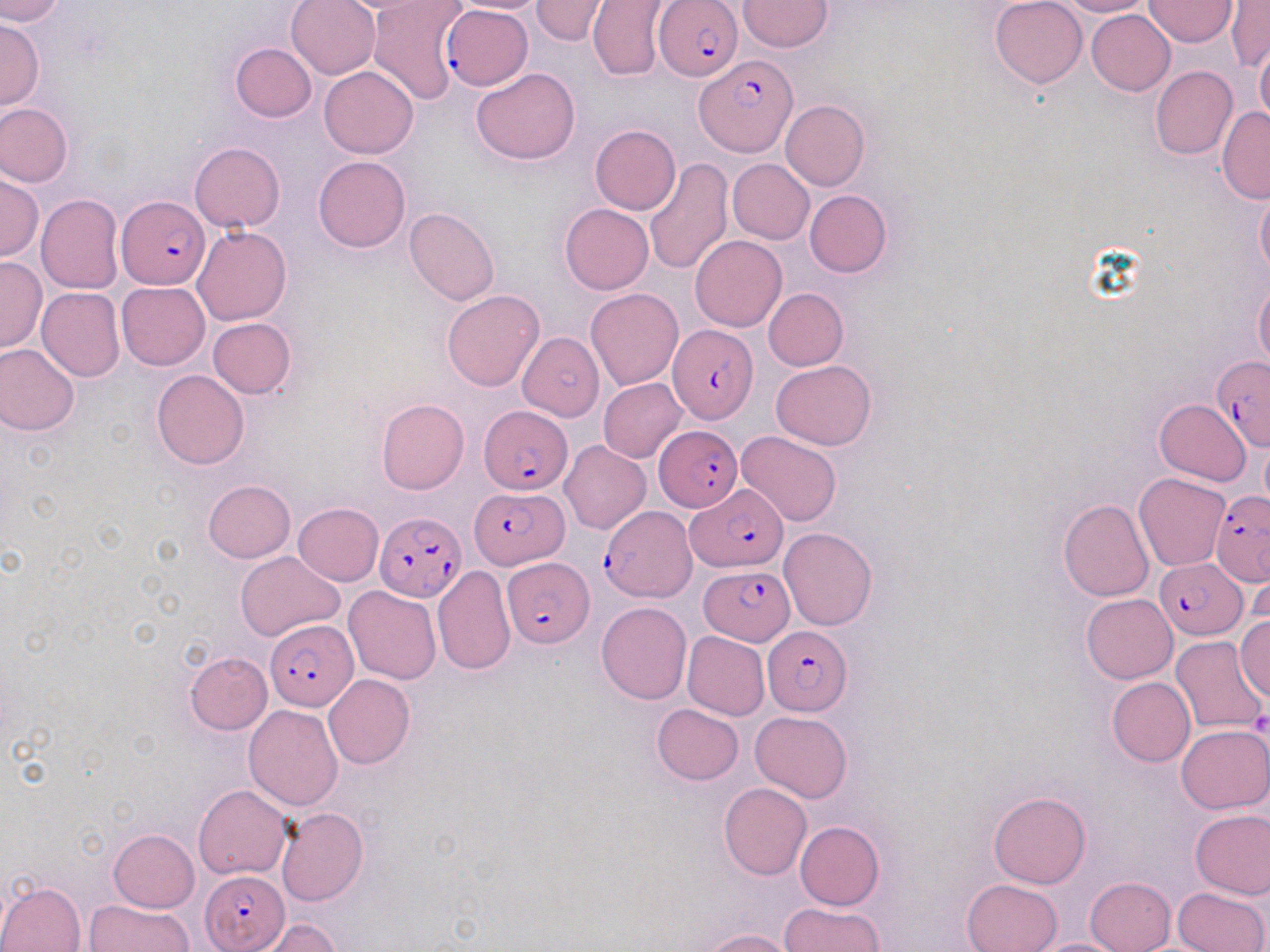

Summary:
  - Coordinate format: approximate bounding boxes as (x1,y1)-(x2,y2) corner pairs in pixels
  - Plasmodium falciparum-infected red blood cell locations: (654,1)-(743,80), (443,6)-(533,92), (695,55)-(795,155), (117,197)-(210,290), (669,325)-(758,423), (1210,357)-(1270,451), (479,406)-(573,494), (653,425)-(742,512), (687,485)-(788,572), (469,486)-(566,568), (1210,491)-(1270,587), (601,505)-(695,600), (375,511)-(466,601), (504,556)-(595,647), (1155,558)-(1245,638), (699,565)-(792,644), (266,619)-(358,709), (762,628)-(851,714), (200,870)-(289,951)
  - Uninfected red blood cell locations: (0,0)-(63,24), (286,0)-(380,79), (325,0)-(450,16), (446,0)-(554,14), (530,0)-(610,44), (588,0)-(674,82), (989,0)-(1087,88), (1053,0)-(1153,16), (366,1)-(468,105), (738,1)-(834,52), (1143,1)-(1235,47), (1226,1)-(1269,73), (1086,10)-(1175,95), (0,18)-(44,111), (234,18)-(376,103), (1255,39)-(1270,126), (229,43)-(316,122), (1150,65)-(1237,160), (319,66)-(418,159), (471,68)-(581,165), (781,100)-(869,192), (0,103)-(73,188), (1217,107)-(1269,203), (590,125)-(680,215), (189,142)-(285,232), (313,155)-(410,252), (644,158)-(733,274), (727,159)-(814,244), (0,173)-(42,261), (1255,186)-(1270,282), (803,189)-(892,278), (36,195)-(125,294), (560,204)-(653,294), (405,207)-(500,308), (192,226)-(291,325), (690,234)-(786,331), (0,258)-(48,352), (116,281)-(210,370), (1254,281)-(1270,367), (37,287)-(124,381), (585,288)-(683,390), (763,288)-(848,370), (442,290)-(545,392), (207,318)-(296,398), (520,330)-(606,432), (0,342)-(79,436), (770,361)-(876,450), (151,369)-(249,469), (598,377)-(687,463), (1154,398)-(1250,485), (376,399)-(469,494), (736,431)-(842,528), (1261,439)-(1270,512), (561,440)-(651,534), (1134,473)-(1229,571), (203,479)-(295,562), (1059,500)-(1155,601), (292,502)-(383,586), (780,527)-(878,630), (236,551)-(343,642), (432,566)-(517,675), (1244,569)-(1267,641), (343,585)-(441,685), (1081,594)-(1178,684), (596,602)-(692,705), (1236,614)-(1270,701), (682,631)-(770,721), (1170,636)-(1268,734), (185,651)-(272,734), (323,674)-(415,769), (1107,677)-(1196,766), (653,703)-(743,784), (243,705)-(344,810), (750,711)-(852,801), (737,712)-(836,873), (1176,724)-(1270,813), (719,782)-(812,880), (194,785)-(292,880), (988,790)-(1090,888), (276,807)-(368,907), (1190,810)-(1270,897), (794,821)-(884,910), (108,829)-(200,912), (1085,877)-(1176,952), (961,879)-(1062,952), (0,880)-(86,951), (1175,887)-(1268,952), (84,899)-(192,952), (780,902)-(884,952), (261,919)-(340,952), (702,929)-(796,952), (1025,938)-(1135,952)
  - Platelet locations: (1250,711)-(1270,738)
  - Slide-level diagnosis: Plasmodium falciparum
  - Field of view: one of a larger specimen
  - Preparation: thin blood smear
  - Image size: 1270×952 pixels
  - Magnification: 1000x
  - Stain: May-Grünwald-Giemsa
  - Modality: optical microscopy